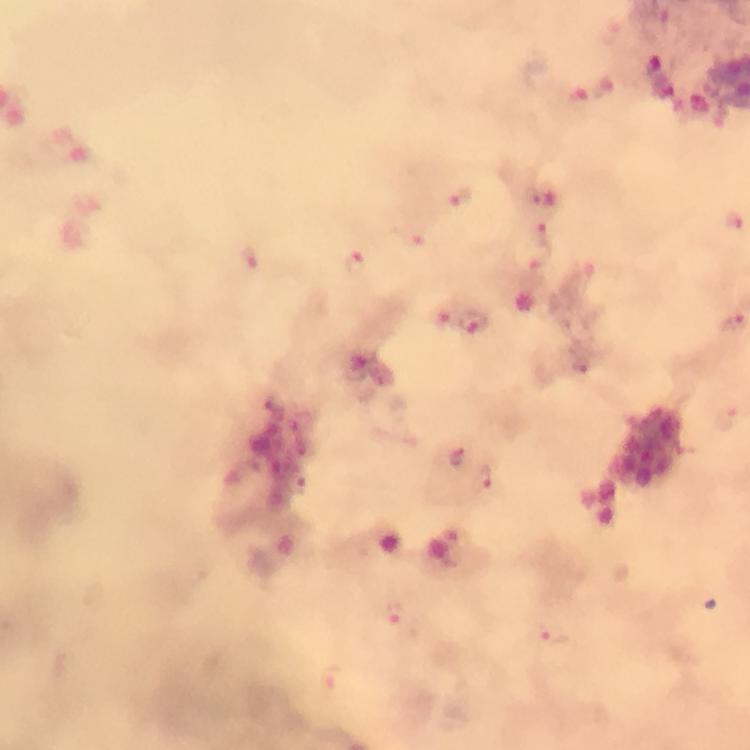
immersion oil = applied
context = from a diagnostic examination for malaria
cropped from = one field of view
capture = smartphone mounted on the microscope
preparation = thick smear
magnification = 100x
malaria parasite locations = approximate object centers, in pixels from the top-left corner: (x=664, y=87), (x=577, y=98), (x=545, y=195), (x=462, y=200), (x=733, y=222), (x=544, y=236), (x=419, y=244), (x=249, y=260), (x=356, y=266), (x=580, y=281), (x=475, y=323), (x=580, y=366), (x=727, y=419), (x=458, y=457), (x=483, y=479), (x=298, y=483), (x=395, y=616), (x=550, y=634), (x=328, y=677)
stain = Giemsa
image size = 750×750 pixels